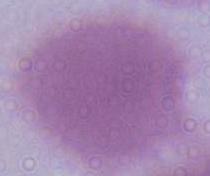 Captured at 1000x magnification. An erythrocyte is shown. Micrograph.